Identify the preparation type.
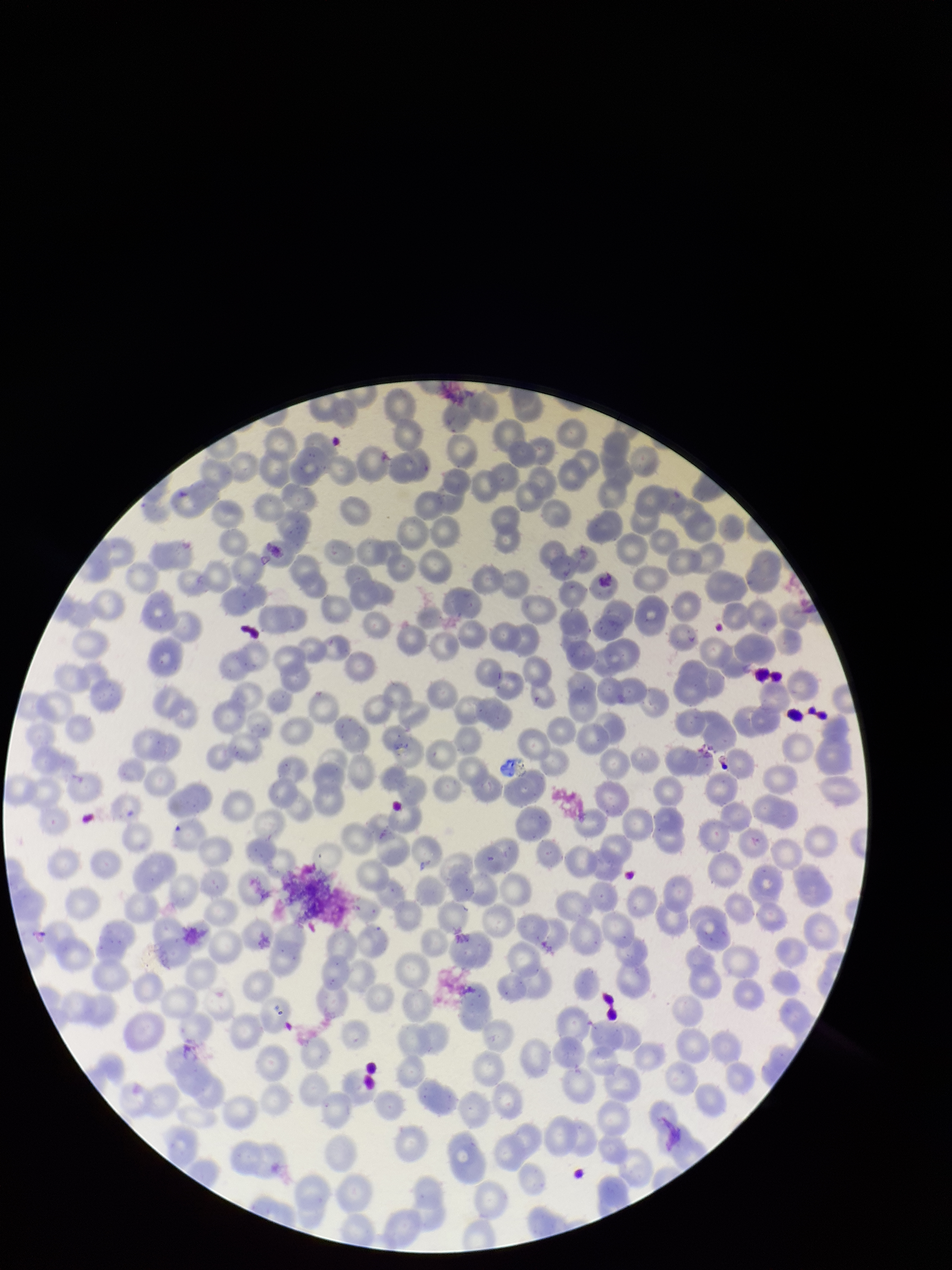

Thin.

Species reported for this patient: Plasmodium vivax. Patient malaria status: positive. Parasitized red blood cells: none identified. Red blood cell count: 218. Parasitized red blood cell count: 0. Image is 952×1270 pixels. Smartphone photograph taken through the eyepiece of a microscope. Giemsa stain. One field from this slide.